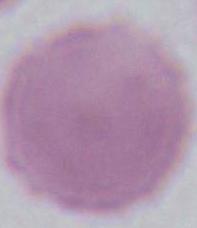
identification = red blood cell
modality = photomicrograph
magnification = 1000x